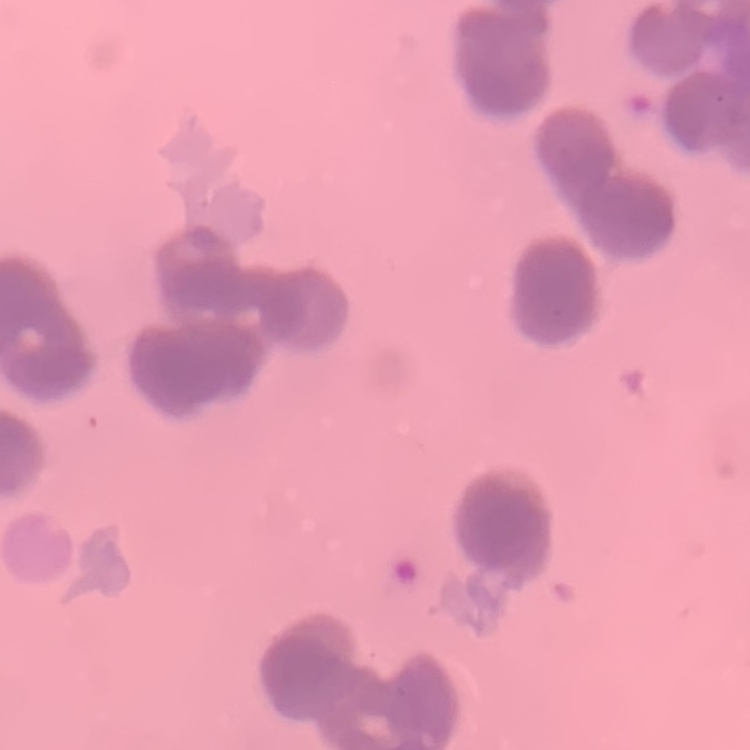
Summary:
  - Red blood cell morphology: rouleaux formation
  - Image type: square crop of a larger photomicrograph
  - Preparation: thin blood smear
  - Stain: Field's or Giemsa